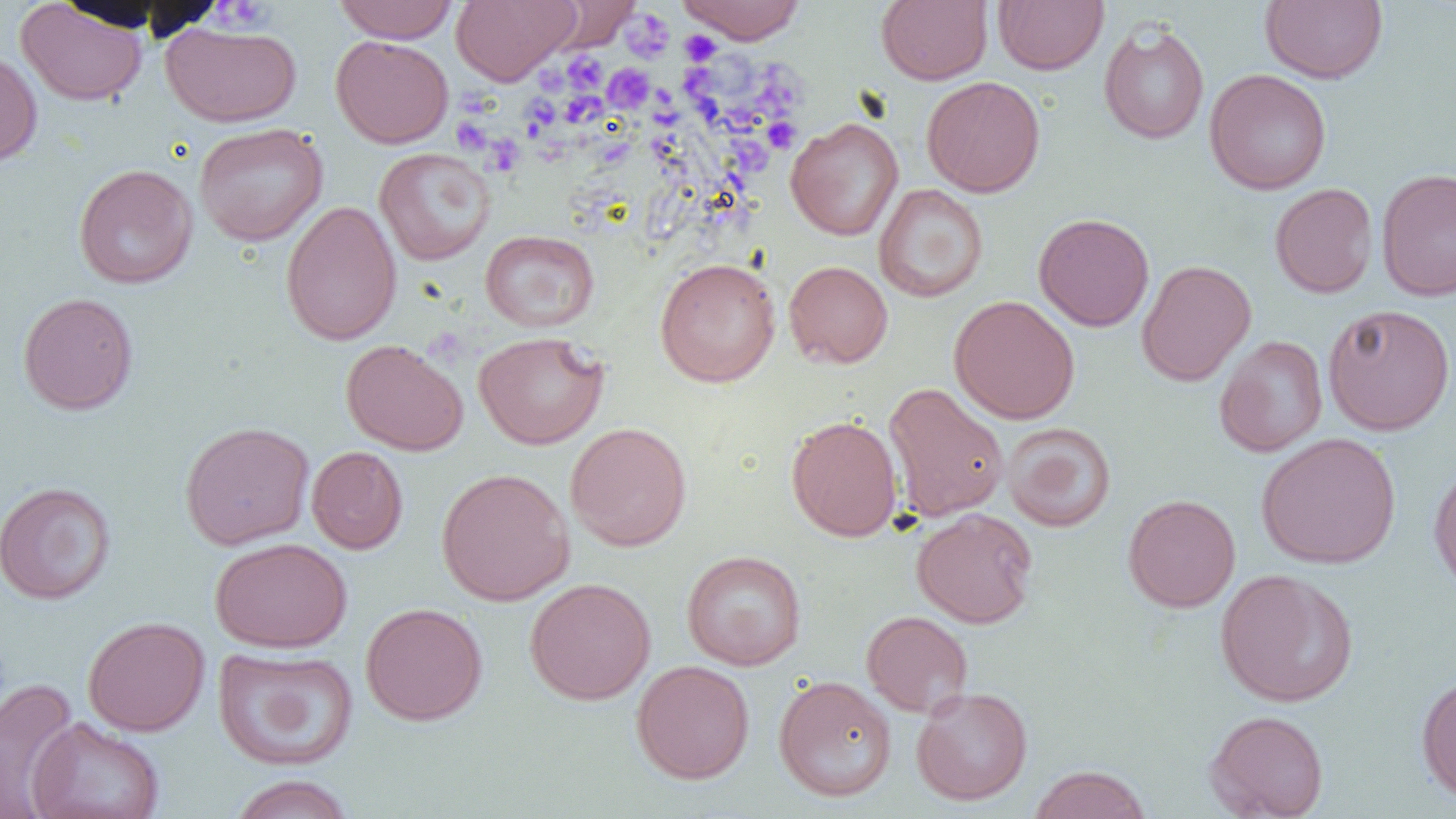
Approximate bounding boxes as (x1, y1, x2, y2) in pixels. Uninfected red blood cell locations: (332, 0, 460, 43), (451, 0, 578, 85), (675, 0, 808, 44), (876, 0, 993, 85), (1260, 0, 1388, 84), (15, 1, 148, 106), (546, 1, 640, 50), (994, 1, 1108, 75), (161, 21, 303, 127), (1098, 21, 1210, 144), (330, 35, 454, 148), (0, 49, 43, 168), (1204, 68, 1332, 195), (921, 76, 1045, 197), (786, 117, 904, 241), (193, 122, 328, 246), (374, 147, 495, 265), (73, 164, 198, 289), (1376, 167, 1456, 301), (873, 183, 989, 303), (1269, 183, 1378, 298), (281, 200, 402, 346), (1033, 212, 1155, 332), (480, 230, 599, 332), (654, 257, 781, 387), (1136, 259, 1256, 386), (784, 260, 893, 368), (17, 292, 139, 415), (949, 295, 1081, 424), (1323, 303, 1455, 435), (474, 331, 609, 449), (1214, 335, 1328, 457), (340, 339, 468, 455), (883, 382, 1009, 522), (786, 415, 903, 542), (179, 420, 315, 549), (565, 422, 692, 551), (1002, 422, 1116, 532), (1256, 432, 1401, 569), (306, 446, 408, 554), (1428, 461, 1456, 595), (436, 467, 575, 606), (0, 481, 117, 604), (1123, 494, 1241, 612), (911, 507, 1038, 628), (210, 537, 352, 653), (682, 549, 806, 670), (1215, 568, 1358, 707), (524, 577, 656, 705), (360, 602, 488, 726), (861, 610, 973, 718), (83, 616, 210, 736), (212, 646, 359, 771), (631, 659, 755, 784), (1416, 671, 1456, 805), (774, 674, 896, 802), (1, 678, 80, 815), (912, 685, 1033, 806), (1204, 709, 1330, 819), (26, 717, 165, 819), (1028, 764, 1152, 819), (227, 774, 357, 819). Platelet locations: (210, 1, 274, 32), (622, 9, 675, 62), (678, 30, 722, 65), (562, 52, 606, 94), (743, 61, 814, 124), (605, 64, 653, 113), (678, 72, 720, 104), (562, 91, 606, 128), (653, 92, 681, 131), (520, 95, 560, 135), (451, 116, 492, 154), (770, 125, 810, 148), (482, 133, 524, 177), (593, 139, 637, 170), (735, 140, 775, 174). Slide-level diagnosis: no evidence of blood parasites. Image is 1456×819 pixels. Light microscopy. Single field of view. Captured at 1000x magnification. Thin blood film.